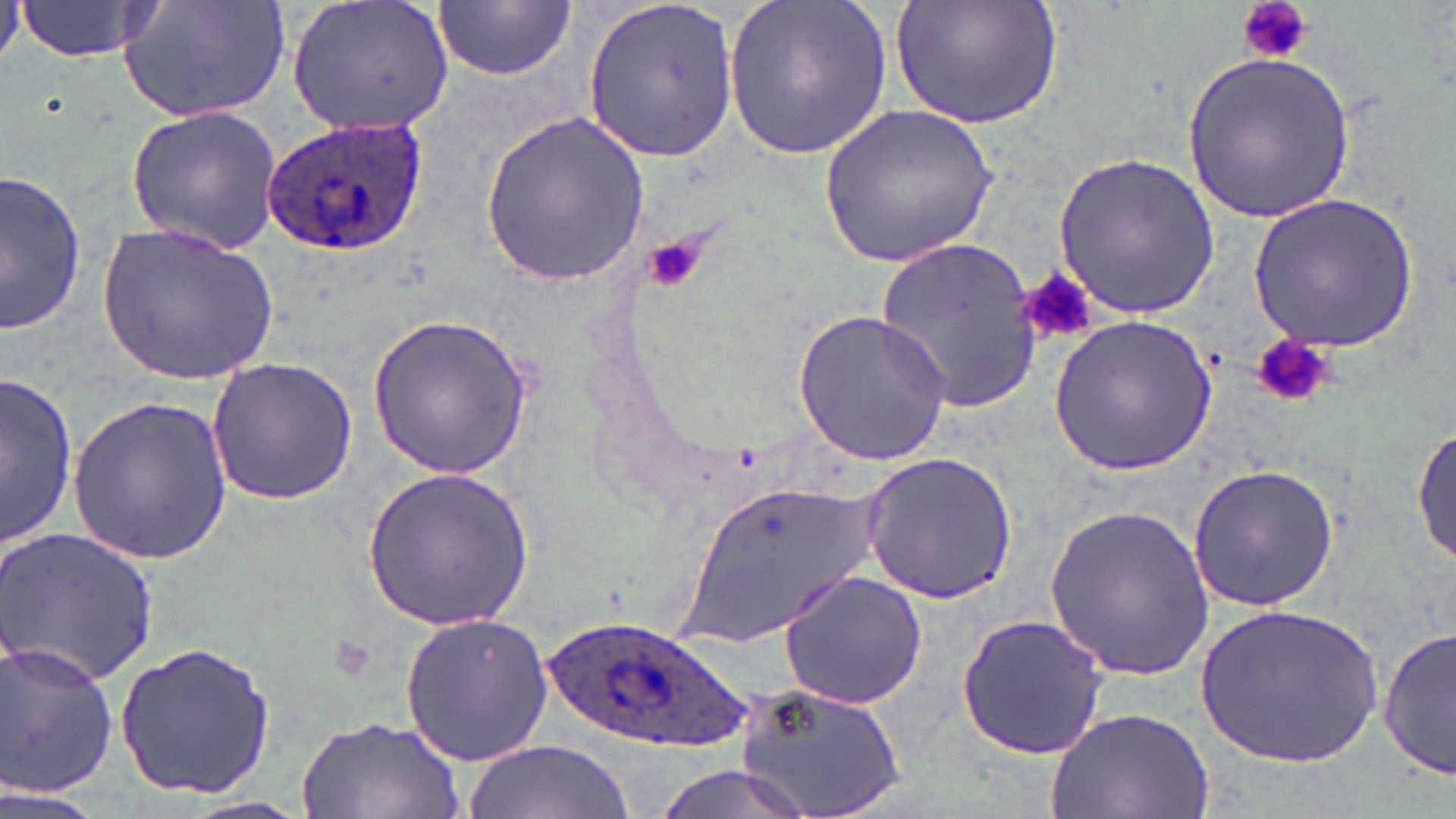

Summary:
  - Coordinate format: approximate bounding boxes as named x1/y1/x2/y2 corners in pixels
  - Plasmodium ovale-infected red blood cell locations: (x1=262, y1=113, x2=429, y2=260), (x1=541, y1=613, x2=764, y2=751)
  - Platelet locations: (x1=1236, y1=0, x2=1314, y2=66), (x1=639, y1=236, x2=706, y2=293), (x1=1020, y1=269, x2=1099, y2=346), (x1=1251, y1=335, x2=1335, y2=411)
  - Uninfected red blood cell locations: (x1=13, y1=0, x2=168, y2=63), (x1=117, y1=0, x2=294, y2=121), (x1=287, y1=0, x2=457, y2=137), (x1=434, y1=0, x2=574, y2=80), (x1=582, y1=0, x2=740, y2=164), (x1=724, y1=0, x2=892, y2=159), (x1=891, y1=0, x2=1063, y2=131), (x1=1182, y1=53, x2=1357, y2=221), (x1=124, y1=102, x2=288, y2=253), (x1=817, y1=102, x2=999, y2=268), (x1=479, y1=110, x2=650, y2=287), (x1=1055, y1=151, x2=1220, y2=320), (x1=1, y1=170, x2=90, y2=337), (x1=1248, y1=191, x2=1421, y2=351), (x1=100, y1=222, x2=279, y2=384), (x1=873, y1=234, x2=1044, y2=415), (x1=791, y1=308, x2=953, y2=465), (x1=368, y1=313, x2=533, y2=479), (x1=1047, y1=316, x2=1216, y2=477), (x1=205, y1=358, x2=358, y2=505), (x1=2, y1=371, x2=80, y2=549), (x1=69, y1=393, x2=233, y2=563), (x1=1412, y1=425, x2=1455, y2=566), (x1=859, y1=450, x2=1021, y2=605), (x1=362, y1=463, x2=536, y2=631), (x1=1186, y1=463, x2=1339, y2=611), (x1=684, y1=477, x2=880, y2=651), (x1=1043, y1=500, x2=1214, y2=681), (x1=0, y1=526, x2=161, y2=686), (x1=777, y1=569, x2=927, y2=707), (x1=1195, y1=602, x2=1384, y2=770), (x1=399, y1=610, x2=554, y2=766), (x1=956, y1=615, x2=1108, y2=759), (x1=1378, y1=624, x2=1456, y2=784), (x1=114, y1=639, x2=278, y2=800), (x1=0, y1=641, x2=120, y2=798), (x1=732, y1=682, x2=911, y2=817), (x1=1044, y1=706, x2=1215, y2=819), (x1=296, y1=715, x2=466, y2=819), (x1=464, y1=739, x2=632, y2=819), (x1=646, y1=764, x2=826, y2=819), (x1=0, y1=789, x2=107, y2=819)
  - Slide-level diagnosis: Plasmodium ovale
  - Field of view: one of a larger specimen
  - Stain: May-Grünwald-Giemsa
  - Image size: 1456×819 pixels
  - Preparation: thin blood film
  - Magnification: 1000x
  - Modality: optical microscopy